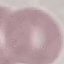

Summary:
  - Malaria status: uninfected
  - Preparation: thin blood film
  - Image type: automatically extracted cell patch, resized to 64 × 64 pixels
  - Stain: Giemsa
  - Capture: smartphone camera at the microscope eyepiece